Report the malaria status of this cell.
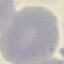
Uninfected.

Photographed with a smartphone camera at the microscope eyepiece. Giemsa-stained preparation. Thin blood smear. Cell patch, automatically extracted from a larger field of view and resized to 64 × 64 pixels.